Name the parasite shown.
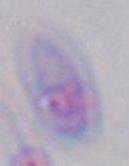
Toxoplasma gondii.

magnification: 1000x
modality: micrograph